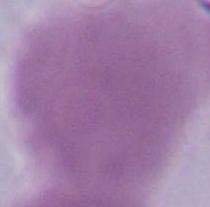

Summary:
  - Modality: micrograph
  - Identification: red blood cell
  - Magnification: 1000x